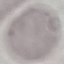
Summary:
  - Result: no malaria parasites seen
  - Preparation: thin smear
  - Capture: smartphone camera at the microscope eyepiece
  - Image type: cell patch, automatically extracted from a larger field of view and resized to 64 × 64 pixels
  - Stain: Giemsa